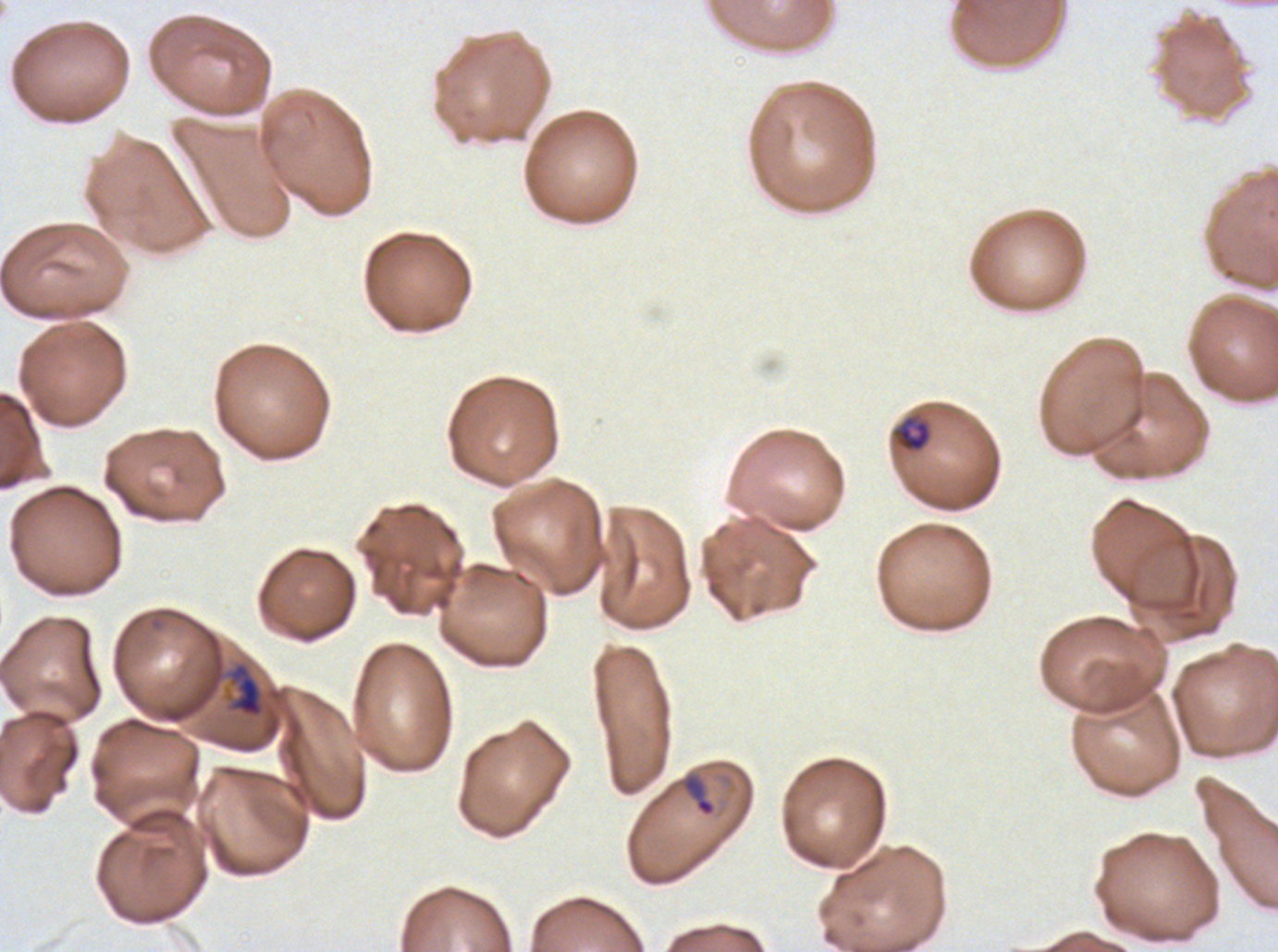 Approximate bounding boxes as (x1, y1, x2, y2) in pixels. Late-ring/early-trophozoite locations: (896, 416, 931, 452), (227, 662, 265, 719). Ring locations: (682, 774, 716, 817). Image is 1278×952 pixels. A sub-image separated from a larger composite. P. falciparum from a patient in The Gambia, cultured ex vivo for 24 to 48 hours. Life-cycle stages observed: ring, late-ring/early-trophozoite. Thin blood film. Giemsa stain.